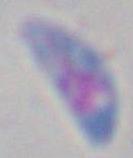
{
  "identification": "Toxoplasma gondii",
  "magnification": "1000x",
  "modality": "photomicrograph"
}